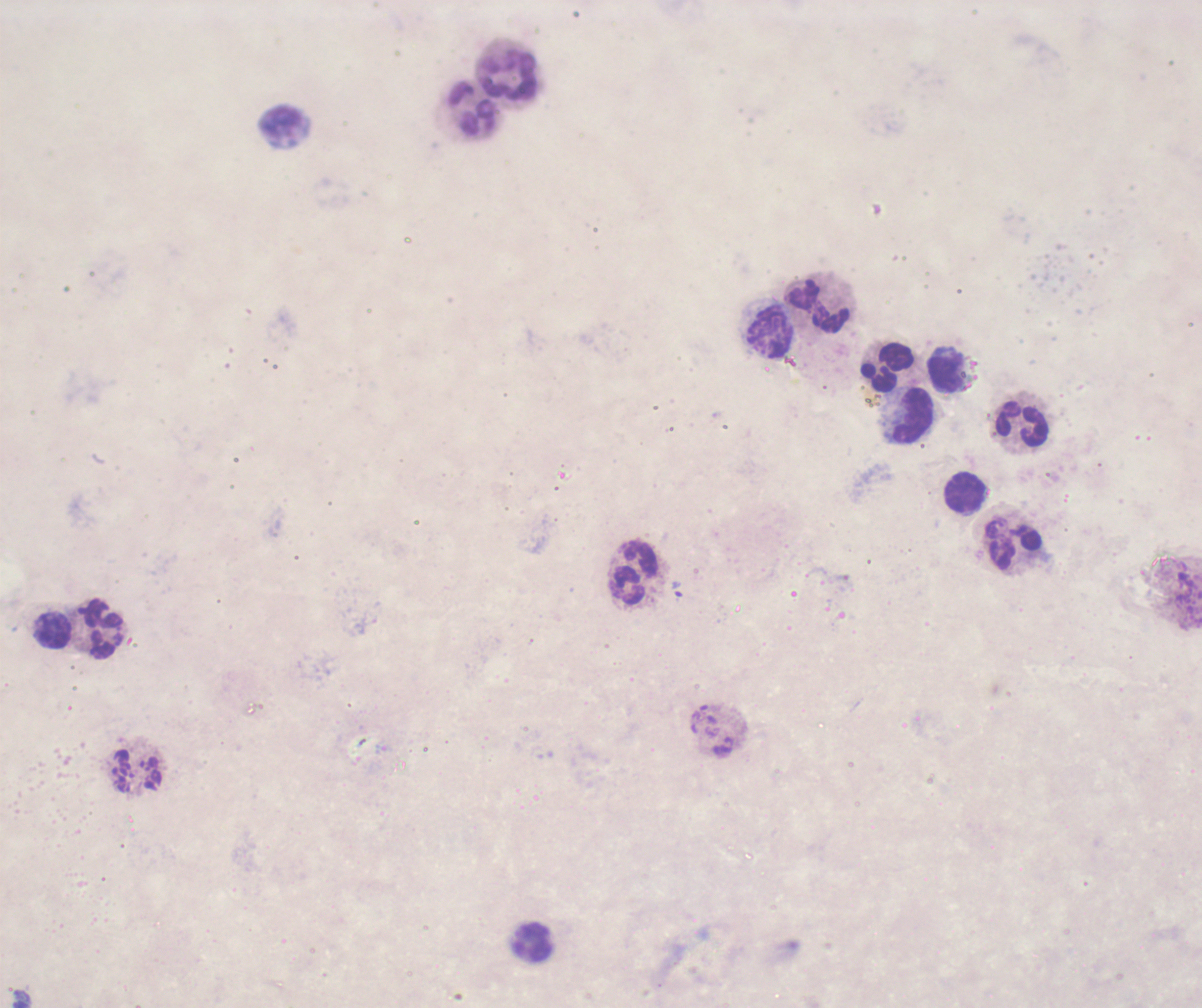

Approximate centers as [x, y] in pixels.
Summary:
  - Leukocyte locations: [509, 76], [473, 108], [281, 120], [820, 305], [770, 333], [889, 366], [944, 372], [915, 416], [1023, 424], [966, 493], [1015, 544], [634, 571], [53, 629], [102, 629], [138, 772], [534, 942]
  - Field of view: single
  - Image size: 1202×1008 pixels
  - Coloration quality: bad
  - Preparation: thick blood smear
  - Magnification: 100x
  - Result: no malaria parasites seen
  - Background quality: poor
  - Context: previously used in an actual diagnosis
  - Stain: Romanowsky